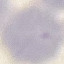

Summary:
  - Malaria status: uninfected
  - Stain: Giemsa
  - Preparation: thin blood smear
  - Image type: automatically extracted cell patch, resized to 64 × 64 pixels
  - Capture: smartphone camera at the microscope eyepiece